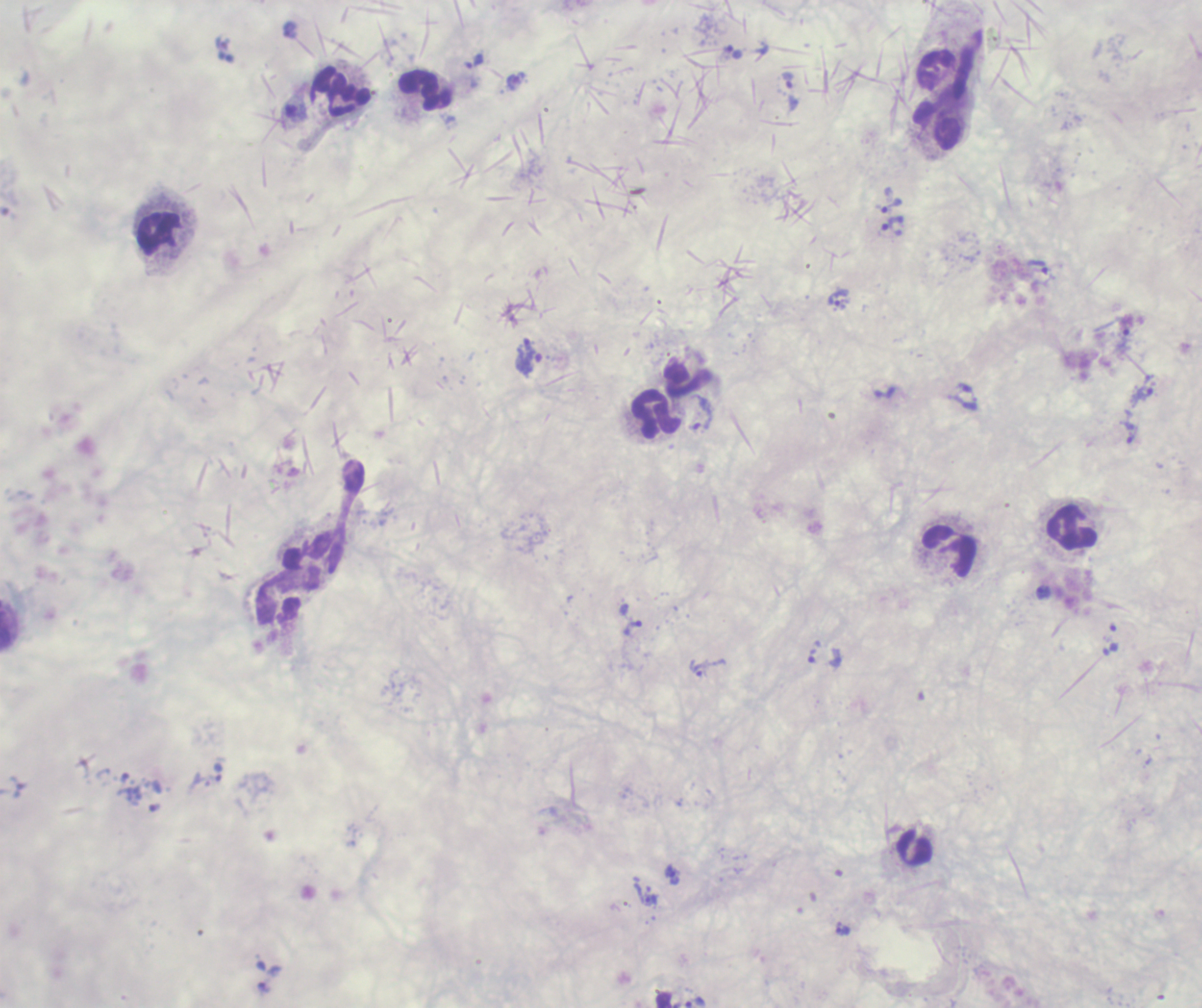

coordinate format = approximate centers as [x, y] in pixels
leukocyte locations = [425, 90], [341, 92], [942, 118], [160, 234], [684, 379], [658, 413], [1074, 527], [324, 551], [949, 552], [915, 849]
trophozoite locations = [734, 52], [474, 61], [788, 80], [516, 81], [891, 205], [893, 226], [1038, 267], [840, 299], [530, 364], [1144, 393], [702, 414], [1132, 436], [1044, 591], [633, 627], [813, 655], [697, 668], [673, 874], [648, 899], [843, 929], [264, 988], [695, 1002]
preparation = thick smear of blood
result = Plasmodium parasites detected
magnification = 100x
field of view = one from this slide
image size = 1202×1008 pixels
stain = Romanowsky
context = previously used in a real diagnosis
background quality = unsatisfactory
coloration quality = bad